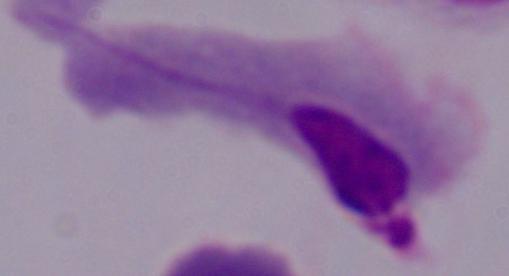
Summary:
  - Modality: photomicrograph
  - Identification: trichomonad
  - Magnification: 1000x